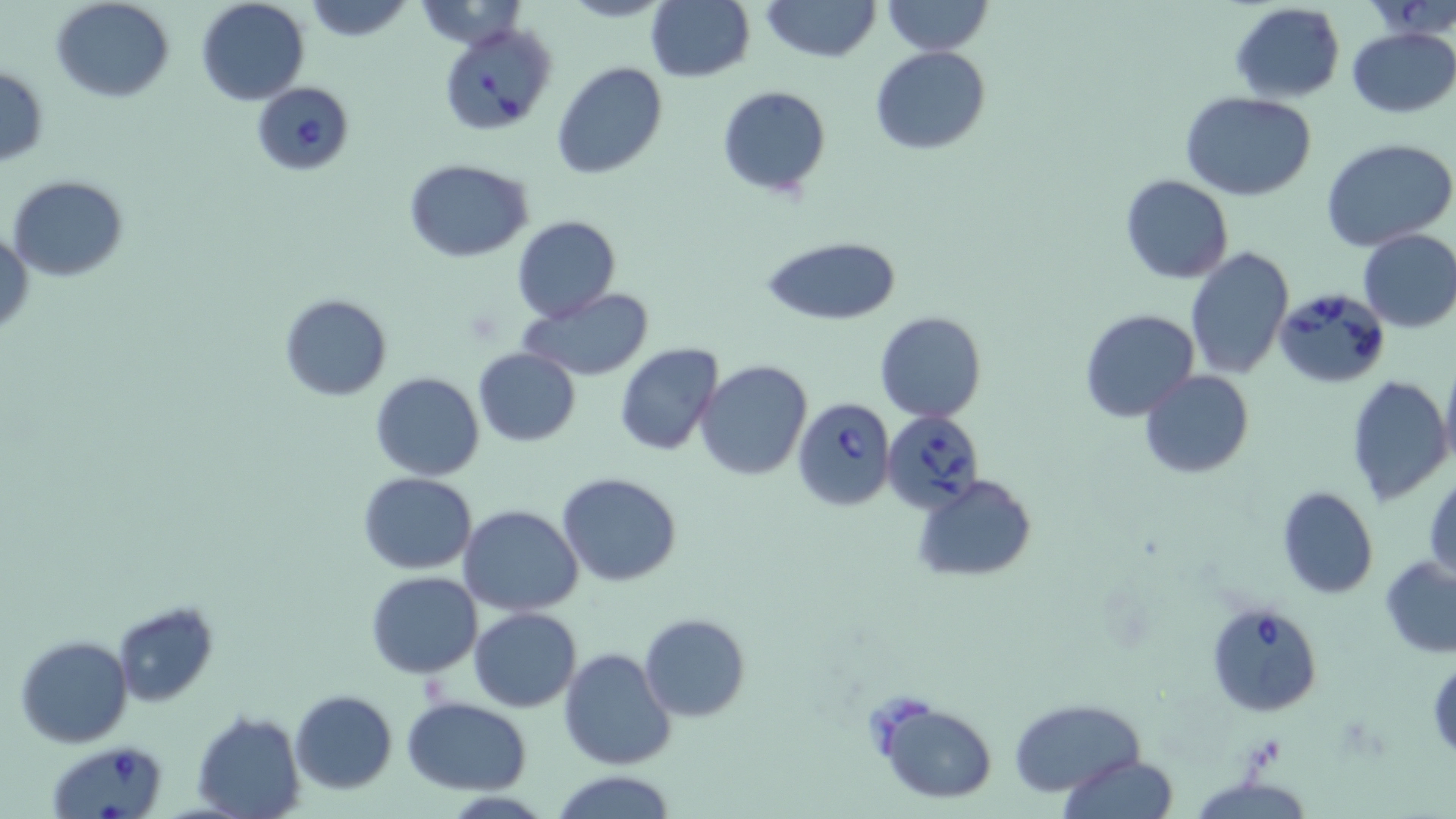
Summary:
  - Coordinate format: approximate bounding boxes as [x1, y1, x2, y2] in pixels
  - Babesia divergens-infected red blood cell locations: [443, 19, 556, 134], [250, 81, 356, 176], [1274, 287, 1388, 391], [793, 396, 895, 511], [881, 410, 984, 513], [1206, 601, 1324, 717], [49, 741, 170, 818]
  - Uninfected red blood cell locations: [52, 0, 174, 102], [195, 0, 309, 106], [300, 0, 417, 42], [762, 0, 879, 62], [881, 0, 992, 55], [646, 1, 754, 82], [1229, 1, 1345, 103], [1347, 27, 1456, 118], [871, 46, 991, 154], [552, 63, 669, 181], [0, 66, 49, 165], [717, 86, 832, 198], [1181, 91, 1316, 200], [1321, 138, 1456, 252], [404, 159, 533, 262], [1120, 175, 1234, 284], [8, 176, 127, 280], [511, 215, 621, 322], [0, 228, 33, 338], [1357, 228, 1456, 333], [761, 235, 901, 327], [1184, 246, 1295, 380], [520, 288, 659, 381], [279, 292, 394, 399], [1080, 308, 1198, 420], [874, 311, 988, 423], [615, 343, 723, 457], [472, 348, 582, 446], [1439, 358, 1456, 477], [697, 360, 813, 480], [1140, 370, 1254, 478], [370, 372, 485, 481], [1345, 374, 1452, 507], [1425, 470, 1456, 584], [358, 472, 478, 574], [556, 473, 683, 587], [913, 473, 1037, 581], [1277, 486, 1378, 598], [459, 505, 584, 616], [1381, 555, 1456, 658], [366, 571, 482, 677], [113, 602, 220, 707], [468, 607, 581, 712], [639, 612, 751, 722], [16, 635, 131, 748], [558, 648, 674, 769], [1427, 654, 1455, 760], [290, 689, 398, 794], [401, 696, 532, 794], [1013, 699, 1142, 797], [875, 700, 997, 803], [191, 711, 305, 819], [1059, 755, 1180, 818], [550, 770, 678, 819]
  - Slide-level diagnosis: Babesia divergens
  - Field of view: single
  - Stain: May-Grünwald-Giemsa
  - Preparation: thin blood film
  - Modality: light microscopy
  - Magnification: 1000x
  - Image size: 1456×819 pixels